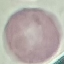

Malaria status: uninfected. Thin blood film. Cell patch, automatically extracted from a larger field of view and resized to 64 × 64 pixels. Acquired by smartphone through the microscope eyepiece. Giemsa-stained preparation.